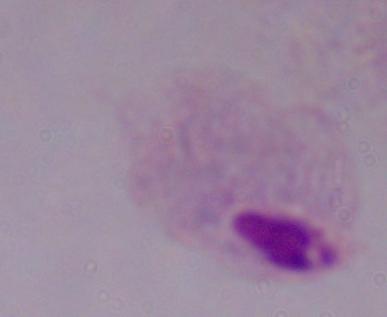
Captured at 1000x magnification. Micrograph. A trichomonad is seen.